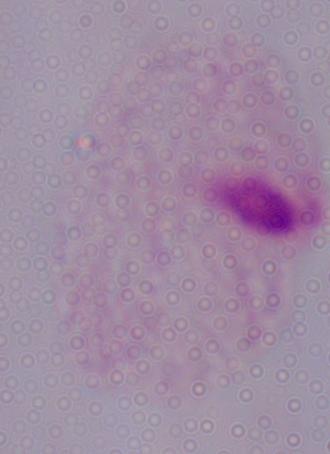
Summary:
  - Magnification: 1000x
  - Modality: micrograph
  - Identification: trichomonad